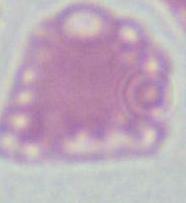

An erythrocyte is seen. Photomicrograph. Captured at 1000x magnification.